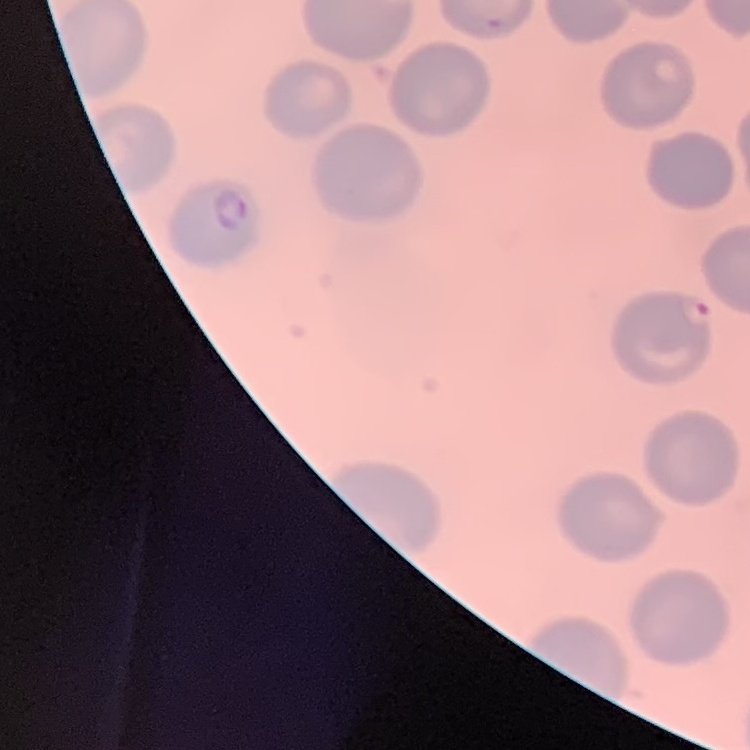
Summary:
  - Erythrocyte morphology: no rouleaux formation
  - Stain: Field's or Giemsa
  - Preparation: thin blood smear
  - Image type: one tile cut from a larger photomicrograph